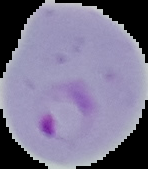

image type = segmented cell region on a black background
image size = 148×169 pixels
preparation = thin blood smear
result = malaria parasites identified